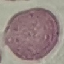

malaria status = uninfected
preparation = thin smear
image type = automatically extracted cell patch, resized to 64 × 64 pixels
capture = smartphone camera at the microscope eyepiece
stain = Giemsa